Mark where platelets are.
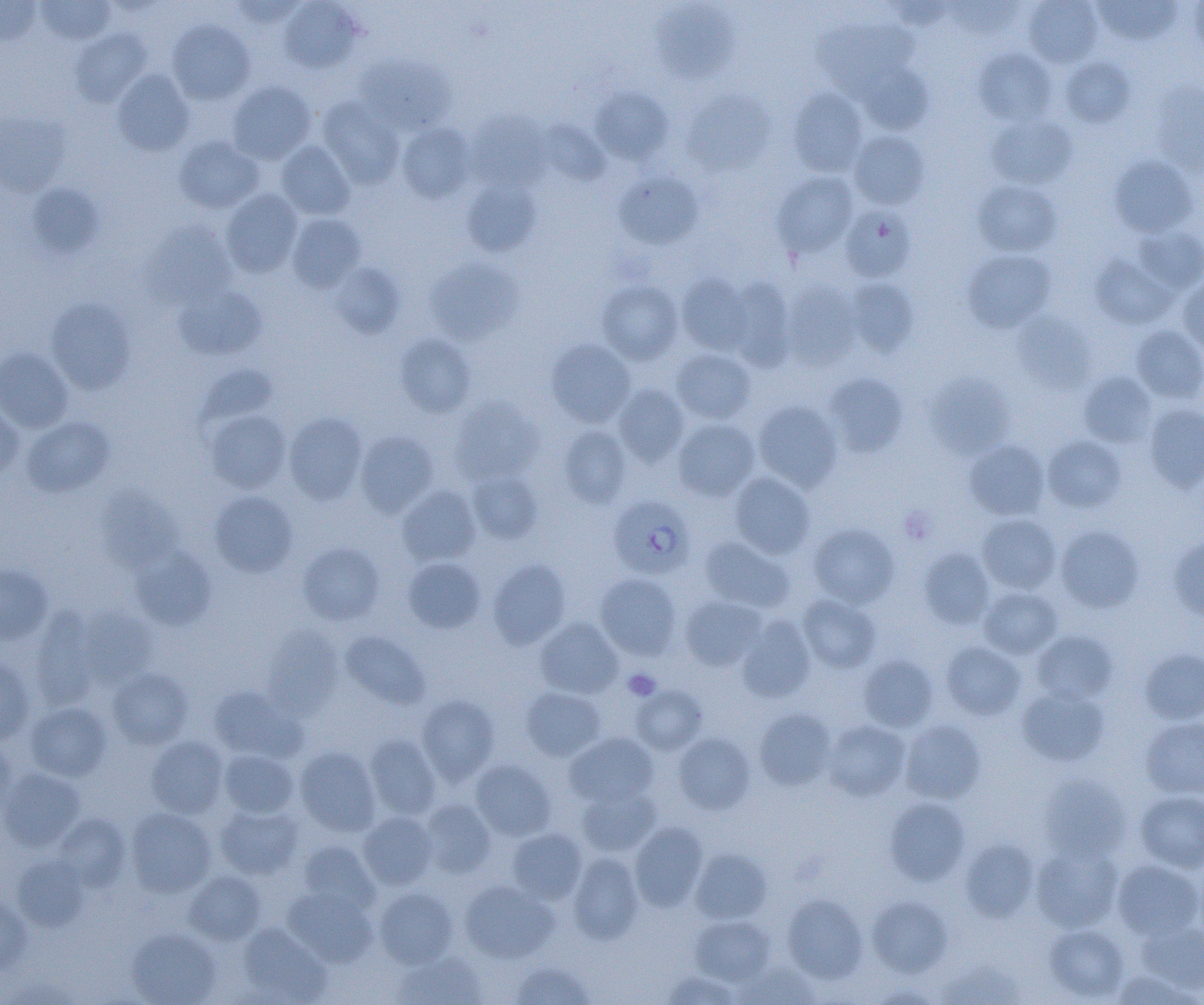
Approximate bounding boxes as [x1, y1, x2, y2] in pixels.
Platelets: [899, 507, 936, 545], [623, 668, 661, 701].

slide-level diagnosis = Plasmodium falciparum
uninfected red blood cell locations = approximate bounding boxes as [x1, y1, x2, y2] in pixels: [0, 0, 41, 45], [228, 0, 307, 27], [1023, 0, 1102, 67], [1189, 0, 1204, 58], [36, 1, 116, 45], [279, 1, 362, 73], [885, 1, 957, 30], [944, 1, 1024, 39], [1093, 1, 1182, 45], [653, 2, 739, 82], [814, 16, 919, 97], [168, 20, 255, 105], [69, 29, 151, 107], [973, 47, 1057, 126], [355, 54, 455, 135], [1059, 56, 1136, 128], [858, 63, 932, 134], [112, 70, 194, 156], [228, 81, 316, 165], [1149, 81, 1204, 174], [590, 87, 673, 164], [682, 88, 776, 175], [787, 88, 867, 177], [318, 97, 404, 189], [466, 110, 552, 191], [0, 112, 70, 196], [987, 114, 1077, 190], [397, 123, 476, 203], [849, 131, 929, 209], [174, 135, 264, 213], [275, 141, 356, 220], [1109, 155, 1197, 238], [613, 171, 703, 249], [773, 172, 858, 258], [461, 179, 541, 257], [973, 180, 1061, 257], [25, 182, 103, 258], [221, 189, 303, 277], [840, 205, 916, 281], [286, 213, 366, 292], [145, 221, 237, 307], [1133, 226, 1204, 294], [962, 250, 1056, 333], [1090, 254, 1176, 329], [425, 258, 524, 345], [328, 262, 404, 338], [677, 273, 754, 356], [726, 277, 796, 370], [1176, 277, 1204, 354], [846, 278, 920, 357], [597, 279, 684, 365], [782, 280, 861, 369], [174, 284, 267, 361], [46, 297, 136, 394], [1012, 313, 1095, 393], [1131, 325, 1204, 403], [395, 332, 477, 417], [546, 339, 636, 427], [0, 347, 74, 433], [671, 349, 756, 424], [194, 363, 278, 432], [1079, 371, 1158, 447], [824, 372, 909, 457], [925, 375, 1015, 460], [613, 383, 689, 466], [450, 395, 544, 484], [753, 401, 843, 492], [1143, 404, 1204, 492], [0, 405, 24, 481], [205, 410, 291, 493], [284, 412, 367, 504], [22, 416, 115, 497], [672, 418, 760, 501], [558, 424, 632, 508], [355, 431, 439, 518], [1042, 435, 1126, 513], [964, 440, 1050, 520], [468, 470, 543, 543], [729, 472, 815, 558], [396, 485, 481, 566], [96, 487, 183, 572], [209, 490, 298, 577], [977, 513, 1061, 594], [808, 523, 899, 608], [1055, 525, 1145, 612], [1169, 534, 1204, 621], [699, 535, 795, 613], [298, 542, 386, 625], [131, 547, 216, 630], [918, 548, 994, 629], [403, 557, 485, 633], [487, 558, 571, 650], [0, 564, 54, 645], [595, 573, 682, 660], [979, 586, 1062, 658], [680, 595, 767, 671], [797, 595, 881, 673], [77, 605, 157, 686], [30, 606, 102, 707], [736, 615, 816, 703], [535, 617, 623, 698], [262, 624, 342, 717], [340, 630, 430, 709], [1032, 630, 1118, 704], [940, 641, 1026, 720], [1140, 648, 1204, 724], [858, 654, 938, 732], [0, 655, 35, 747], [107, 667, 193, 749], [631, 683, 708, 754], [208, 685, 307, 763], [1016, 685, 1110, 767], [521, 687, 606, 760], [416, 694, 500, 785], [25, 702, 112, 781], [754, 708, 836, 790], [1140, 717, 1204, 799], [900, 718, 986, 804], [822, 719, 910, 801], [564, 732, 658, 807], [672, 732, 755, 814], [365, 733, 442, 819], [146, 735, 229, 818], [0, 742, 18, 820], [294, 746, 381, 836], [219, 749, 299, 817], [470, 759, 556, 841], [0, 768, 85, 851], [1039, 774, 1130, 861], [576, 785, 661, 856], [1135, 790, 1204, 872], [884, 797, 971, 885], [420, 799, 496, 878], [215, 803, 303, 879], [126, 808, 215, 897], [358, 811, 438, 889], [53, 813, 131, 890], [630, 822, 708, 911], [507, 828, 587, 904], [959, 838, 1039, 922], [298, 840, 380, 914], [1031, 841, 1123, 932], [690, 848, 772, 923], [567, 852, 644, 944], [10, 854, 89, 932], [1112, 859, 1203, 940], [184, 870, 265, 945], [459, 880, 557, 963], [282, 887, 377, 968], [374, 887, 458, 967], [0, 891, 32, 974], [782, 893, 868, 982], [867, 894, 953, 977], [690, 915, 774, 985], [1137, 922, 1204, 995], [238, 923, 331, 1003], [1043, 924, 1129, 1001], [126, 928, 220, 1005], [390, 953, 487, 1005], [935, 958, 1026, 1005], [510, 960, 595, 1004], [735, 961, 819, 1004], [1110, 969, 1200, 1005], [661, 971, 741, 1005], [866, 982, 943, 1004]
Plasmodium falciparum-infected red blood cell locations = approximate bounding boxes as [x1, y1, x2, y2] in pixels: [607, 495, 695, 581]
field of view = one of a larger specimen
preparation = thin blood smear
modality = light microscopy
magnification = 1000x
image size = 1204×1005 pixels